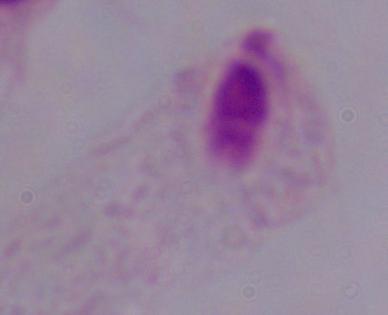 A trichomonad is shown. Micrograph. Captured at 1000x magnification.